Describe the morphology of the erythrocytes.
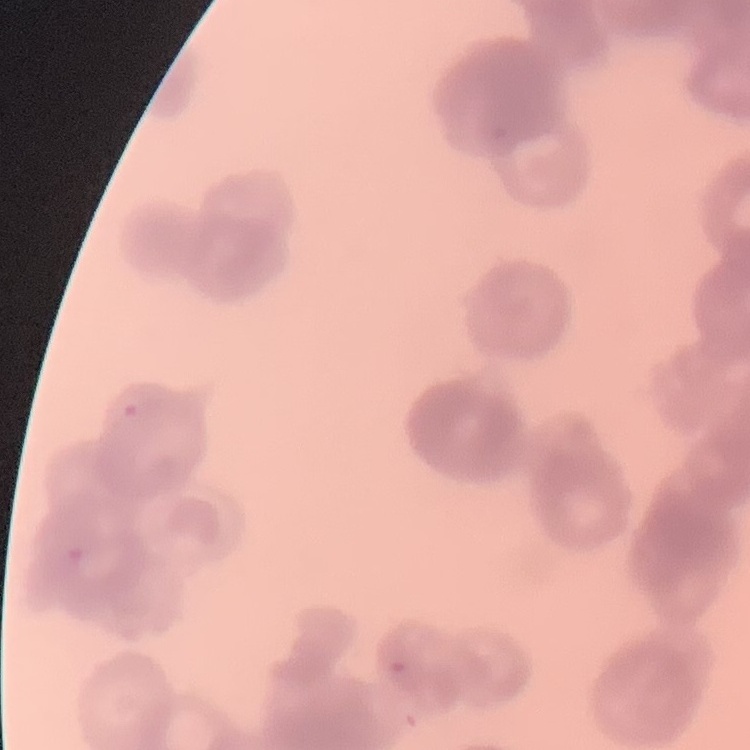
They show rouleaux formation.

Stained with either Field's or Giemsa. One tile cut from a larger photomicrograph. Thin peripheral smear.